Report the malaria status of this cell.
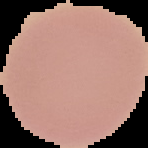

It is uninfected.

Summary:
  - Image type: segmented cell region on a black background
  - Preparation: thin blood film
  - Image size: 148×148 pixels